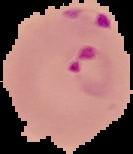
{
  "preparation": "thin blood film",
  "result": "malaria parasites identified",
  "image_type": "segmented cell region with the area outside set to black",
  "image_size": "133×154 pixels"
}